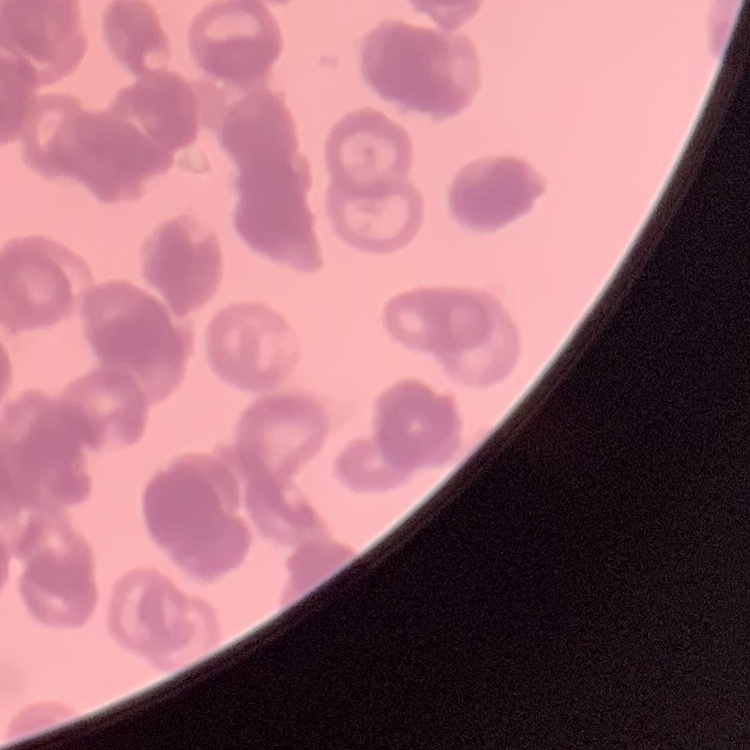 The erythrocytes exhibit rouleaux formation. Thin blood film. Stained with either Field's or Giemsa. One tile cut from a larger photomicrograph.